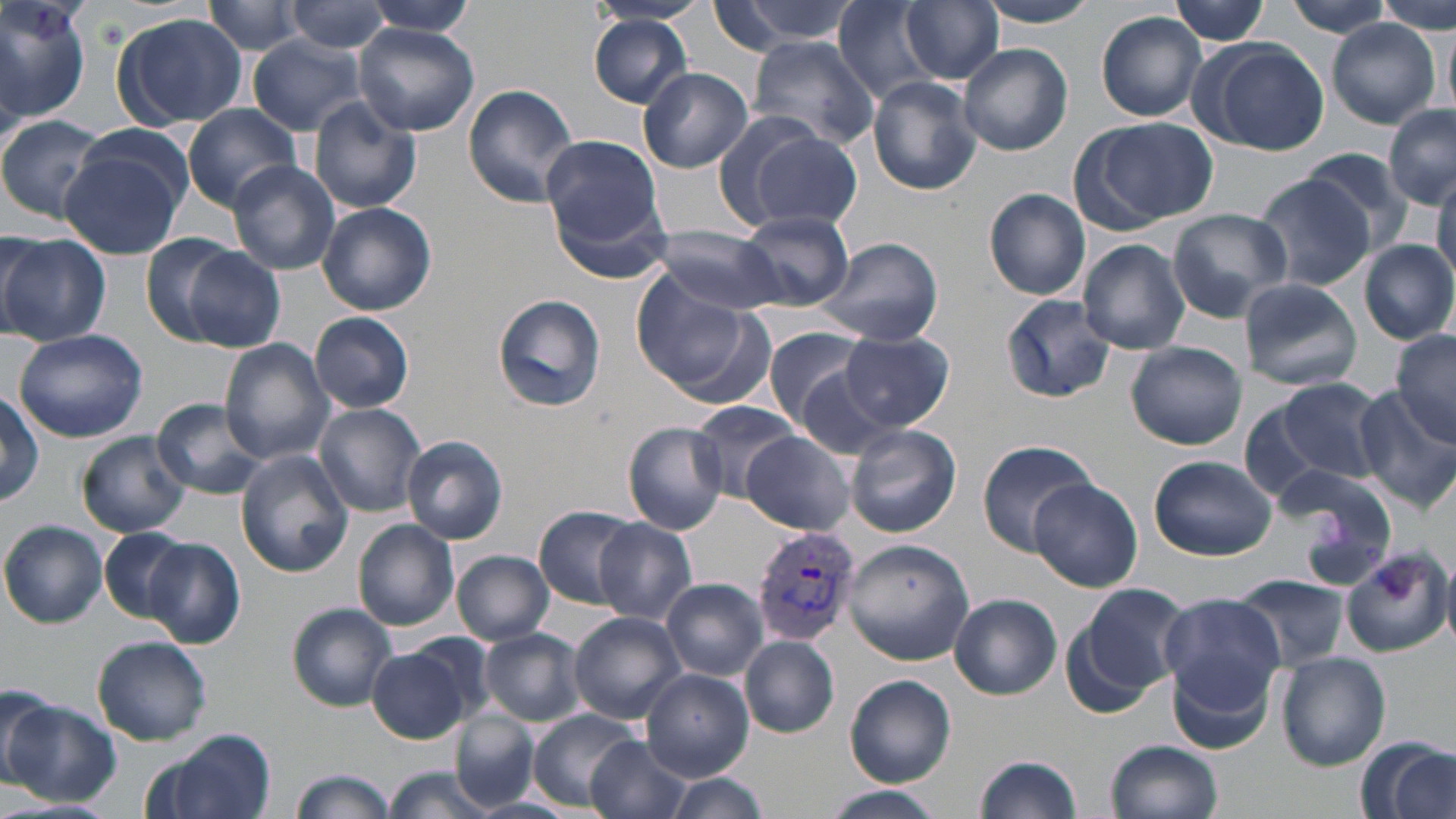

Summary:
  - Coordinate format: approximate bounding boxes as [x1, y1, x2, y2] in pixels
  - Uninfected red blood cell locations: [0, 0, 93, 129], [359, 0, 480, 38], [588, 0, 709, 29], [714, 0, 861, 49], [902, 0, 1003, 84], [976, 0, 1101, 29], [1169, 0, 1271, 44], [1281, 0, 1396, 38], [1376, 0, 1452, 33], [203, 1, 314, 58], [285, 1, 392, 54], [832, 2, 950, 102], [1096, 12, 1207, 122], [111, 13, 248, 131], [588, 16, 694, 107], [1324, 18, 1442, 130], [1440, 18, 1454, 115], [355, 24, 480, 136], [246, 37, 366, 134], [746, 37, 880, 149], [1196, 39, 1330, 156], [956, 42, 1073, 156], [637, 66, 753, 173], [867, 77, 982, 195], [463, 83, 581, 207], [309, 99, 422, 215], [1383, 104, 1456, 211], [183, 105, 304, 210], [0, 114, 109, 225], [1076, 117, 1221, 228], [734, 122, 862, 233], [540, 134, 663, 245], [58, 135, 189, 259], [1298, 148, 1420, 256], [226, 159, 340, 275], [1248, 171, 1377, 292], [1431, 171, 1456, 284], [549, 184, 676, 286], [984, 187, 1091, 300], [317, 202, 437, 315], [1167, 208, 1293, 321], [736, 211, 853, 311], [1100, 220, 1265, 339], [648, 224, 785, 314], [0, 232, 111, 348], [141, 232, 239, 343], [818, 236, 944, 348], [1077, 239, 1191, 355], [1358, 239, 1456, 345], [182, 247, 286, 351], [630, 275, 759, 398], [1238, 279, 1361, 390], [491, 293, 607, 412], [1001, 293, 1115, 404], [310, 312, 414, 413], [761, 325, 874, 429], [1390, 326, 1455, 444], [13, 328, 148, 443], [840, 331, 954, 431], [219, 338, 335, 464], [1126, 341, 1247, 450], [791, 363, 899, 463], [1258, 376, 1389, 495], [1354, 386, 1456, 514], [1, 391, 43, 508], [151, 398, 269, 499], [313, 403, 428, 515], [685, 403, 805, 502], [622, 421, 731, 534], [844, 425, 962, 539], [76, 431, 190, 538], [741, 432, 855, 534], [402, 435, 508, 545], [976, 439, 1098, 554], [236, 451, 353, 576], [1148, 454, 1277, 560], [1273, 466, 1398, 587], [1029, 476, 1143, 592], [536, 505, 641, 609], [593, 518, 696, 625], [353, 519, 460, 632], [1, 521, 107, 628], [99, 528, 191, 624], [840, 537, 976, 666], [145, 538, 244, 648], [1342, 545, 1451, 656], [454, 551, 554, 644], [1235, 574, 1348, 669], [661, 578, 768, 680], [1068, 582, 1193, 706], [1160, 592, 1284, 710], [950, 594, 1061, 699], [287, 603, 398, 711], [568, 611, 686, 724], [479, 629, 585, 726], [93, 635, 212, 745], [740, 636, 839, 738], [368, 643, 477, 744], [1277, 653, 1391, 770], [1167, 657, 1277, 759], [641, 669, 753, 780], [845, 674, 957, 786], [0, 682, 57, 783], [4, 699, 120, 807], [527, 708, 642, 813], [449, 712, 539, 810], [145, 732, 277, 819], [584, 735, 692, 819], [1357, 736, 1456, 819], [1106, 740, 1224, 819], [974, 753, 1082, 819], [385, 766, 497, 819], [291, 767, 395, 819], [663, 774, 769, 818], [823, 788, 945, 819]
  - Plasmodium vivax-infected red blood cell locations: [752, 524, 860, 647]
  - Slide-level diagnosis: Plasmodium vivax
  - Modality: optical microscopy
  - Preparation: thin blood film
  - Stain: May-Grünwald-Giemsa
  - Magnification: 1000x
  - Field of view: one of a larger specimen
  - Image size: 1456×819 pixels